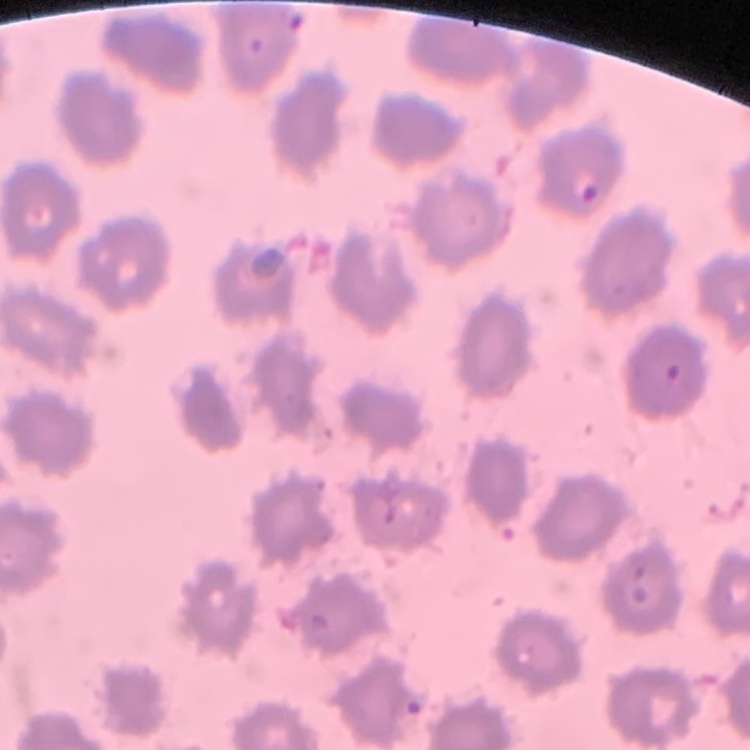

erythrocyte morphology = no rouleaux formation
image type = one tile cut from a larger photomicrograph
preparation = thin peripheral smear
stain = Field's or Giemsa